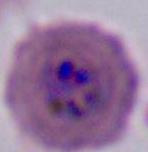
Summary:
  - Magnification: 400x or 1000x
  - Modality: micrograph
  - Identification: Plasmodium